Mark where platelets are.
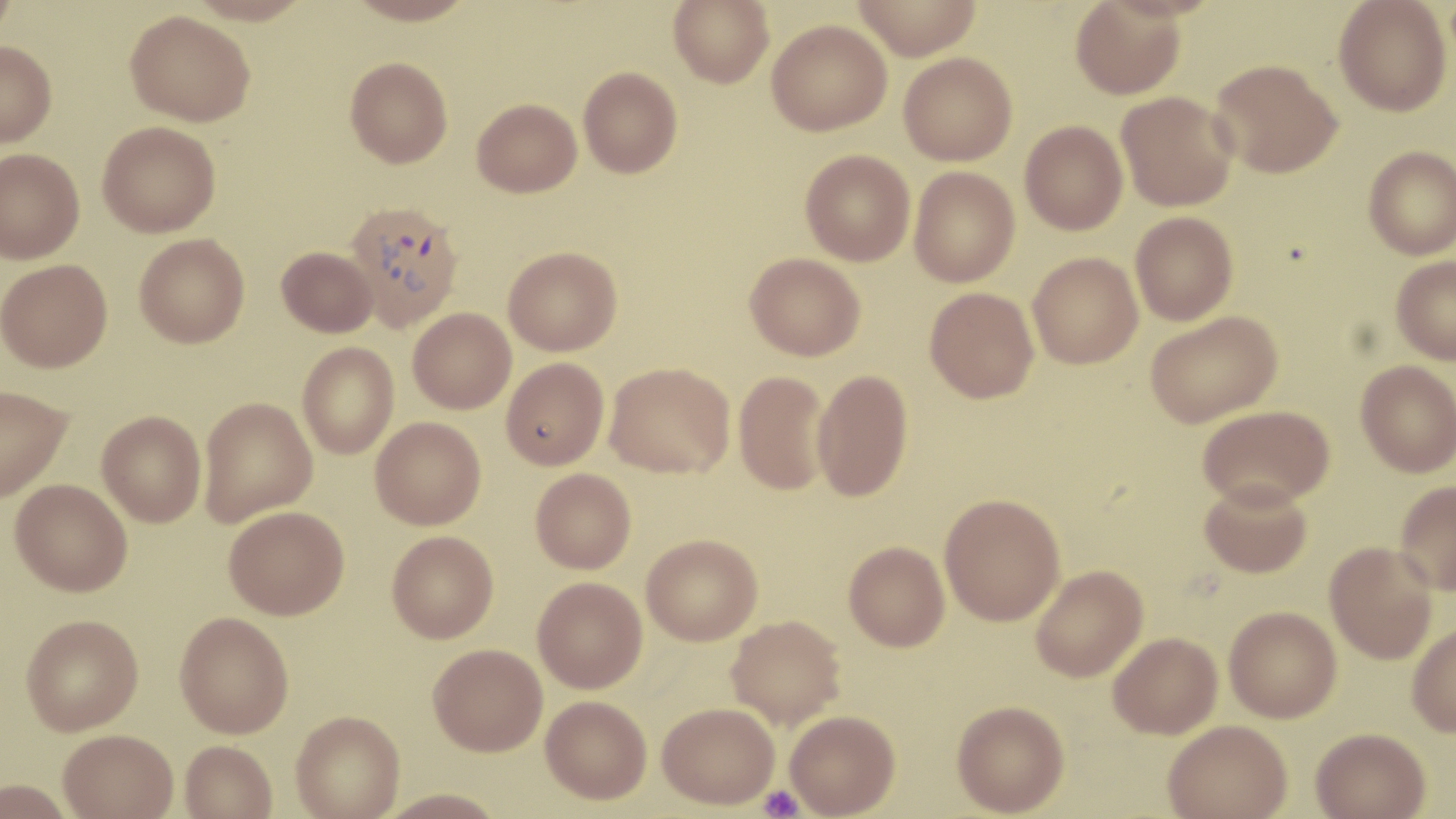

Approximate bounding boxes as (x1, y1, x2, y2) in pixels.
Platelets: (758, 784, 804, 818).

Uninfected red blood cell locations: (0, 0, 17, 47), (186, 0, 314, 26), (344, 0, 478, 26), (668, 0, 774, 87), (850, 0, 982, 60), (1333, 0, 1451, 116), (1070, 1, 1186, 99), (125, 10, 255, 126), (767, 18, 892, 135), (0, 40, 57, 146), (898, 52, 1018, 166), (344, 56, 453, 168), (1210, 59, 1342, 178), (578, 66, 682, 178), (1116, 91, 1239, 211), (472, 97, 582, 197), (1020, 120, 1128, 235), (97, 121, 221, 237), (1364, 147, 1456, 259), (0, 148, 85, 263), (800, 149, 915, 266), (909, 167, 1020, 287), (1130, 211, 1238, 325), (134, 233, 250, 348), (504, 245, 622, 356), (276, 246, 377, 337), (745, 252, 865, 361), (1028, 252, 1143, 369), (1391, 256, 1456, 365), (0, 259, 112, 372), (925, 287, 1039, 403), (408, 308, 516, 413), (1145, 310, 1282, 427), (298, 342, 399, 459), (500, 357, 609, 470), (1355, 360, 1456, 477), (604, 362, 734, 478), (812, 369, 913, 502), (734, 370, 832, 496), (0, 385, 72, 502), (199, 397, 318, 526), (1197, 405, 1334, 509), (96, 411, 206, 527), (370, 416, 486, 529), (530, 468, 636, 574), (9, 478, 132, 596), (1199, 479, 1313, 578), (1394, 481, 1456, 596), (939, 493, 1066, 625), (224, 505, 349, 619), (387, 531, 498, 643), (642, 533, 762, 645), (843, 540, 950, 651), (1325, 541, 1438, 665), (1030, 564, 1148, 682), (532, 577, 647, 693), (1224, 605, 1342, 722), (174, 611, 294, 738), (21, 614, 144, 735), (726, 615, 846, 730), (1407, 621, 1456, 737), (1108, 631, 1223, 738), (428, 643, 547, 756), (541, 695, 652, 804), (951, 700, 1070, 816), (657, 702, 779, 809), (290, 709, 405, 818), (785, 710, 900, 818), (1163, 719, 1292, 818), (1311, 727, 1431, 819), (58, 728, 178, 819), (180, 740, 277, 819), (1, 779, 76, 818), (375, 788, 507, 817). Plasmodium vivax-infected red blood cell locations: (343, 200, 465, 331). Slide-level diagnosis: Plasmodium vivax. May-Grünwald-Giemsa stain. Thin blood smear. Light microscopy. Captured at 1000x magnification. Image is 1456×819 pixels. Single field of view.